Outline each blood parasite and name the species.
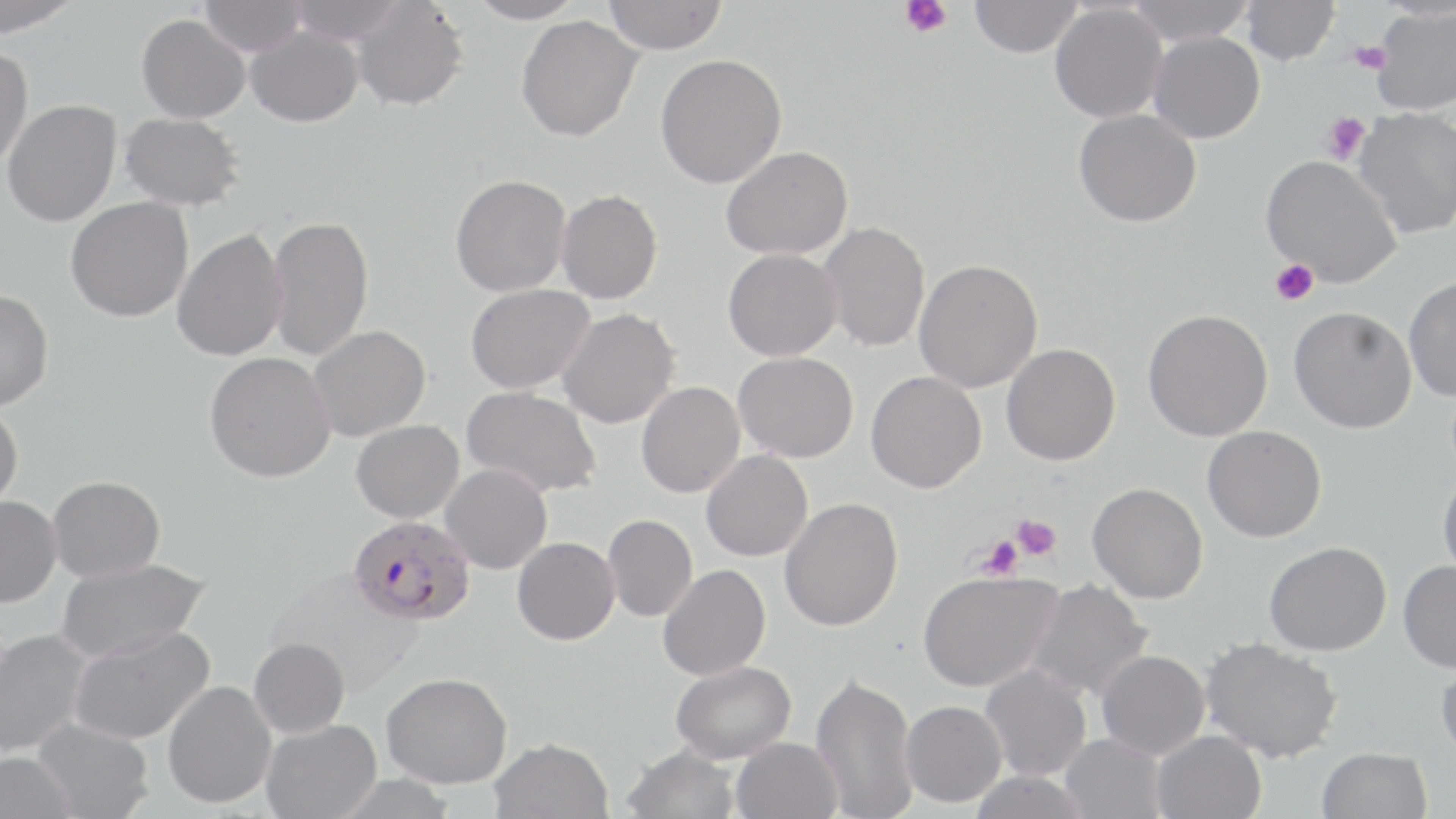

Approximate bounding boxes as [x1, y1, x2, y2] in pixels.
Plasmodium falciparum-infected red blood cells: [348, 514, 476, 626].
No Plasmodium ovale, Plasmodium malariae, Plasmodium vivax, Babesia divergens, or Trypanosoma brucei observed.

Uninfected red blood cell locations: [0, 0, 83, 36], [199, 0, 306, 56], [286, 0, 407, 44], [466, 0, 585, 24], [603, 0, 728, 54], [969, 0, 1082, 57], [1127, 0, 1255, 46], [351, 1, 468, 111], [1240, 1, 1340, 66], [1049, 4, 1167, 123], [1371, 6, 1456, 115], [137, 14, 250, 123], [515, 15, 642, 142], [244, 26, 363, 127], [1147, 31, 1265, 144], [0, 46, 33, 170], [655, 53, 786, 189], [2, 99, 121, 227], [1352, 107, 1456, 239], [1073, 109, 1201, 227], [119, 112, 244, 211], [720, 145, 854, 260], [1261, 155, 1402, 288], [449, 174, 571, 297], [555, 189, 662, 304], [65, 196, 193, 322], [267, 214, 373, 362], [818, 221, 930, 352], [171, 228, 288, 361], [723, 248, 842, 361], [912, 258, 1043, 393], [1403, 277, 1456, 401], [465, 283, 594, 394], [0, 289, 54, 411], [1288, 305, 1417, 433], [557, 308, 680, 428], [1142, 308, 1273, 442], [308, 325, 430, 442], [1001, 343, 1120, 465], [204, 351, 335, 482], [733, 351, 857, 463], [865, 371, 986, 493], [636, 381, 745, 497], [462, 386, 602, 498], [0, 402, 23, 515], [351, 420, 464, 523], [1202, 425, 1326, 542], [700, 449, 812, 561], [440, 464, 552, 574], [1437, 469, 1456, 584], [47, 475, 165, 582], [1087, 482, 1207, 603], [0, 495, 61, 607], [779, 497, 903, 631], [602, 514, 696, 622], [512, 537, 619, 645], [1263, 542, 1391, 656], [55, 558, 211, 663], [1398, 560, 1456, 673], [657, 564, 770, 680], [266, 568, 423, 696], [917, 570, 1061, 693], [1023, 579, 1153, 703], [68, 625, 214, 744], [0, 629, 92, 758], [248, 637, 350, 738], [1200, 638, 1342, 763], [1096, 650, 1209, 759], [1436, 656, 1456, 765], [670, 660, 796, 763], [980, 664, 1091, 781], [811, 671, 918, 818], [381, 672, 511, 787], [163, 680, 277, 809], [899, 700, 1006, 807], [32, 717, 153, 819], [261, 720, 382, 819], [1151, 730, 1266, 819], [1061, 733, 1166, 819], [489, 737, 613, 819], [731, 737, 843, 819], [621, 745, 742, 819], [1316, 747, 1433, 819], [0, 752, 78, 819], [967, 770, 1090, 819]. Platelet locations: [898, 0, 952, 38], [1347, 41, 1391, 73], [1320, 111, 1371, 165], [1271, 259, 1319, 306], [1011, 514, 1061, 561], [976, 535, 1023, 581]. Slide-level diagnosis: Plasmodium falciparum. Optical microscopy. May-Grünwald-Giemsa-stained preparation. 1000x magnification. One field of a larger specimen. Thin blood smear. Image is 1456×819 pixels.